Give the extent of all Plasmodium falciparum-infected red blood cells.
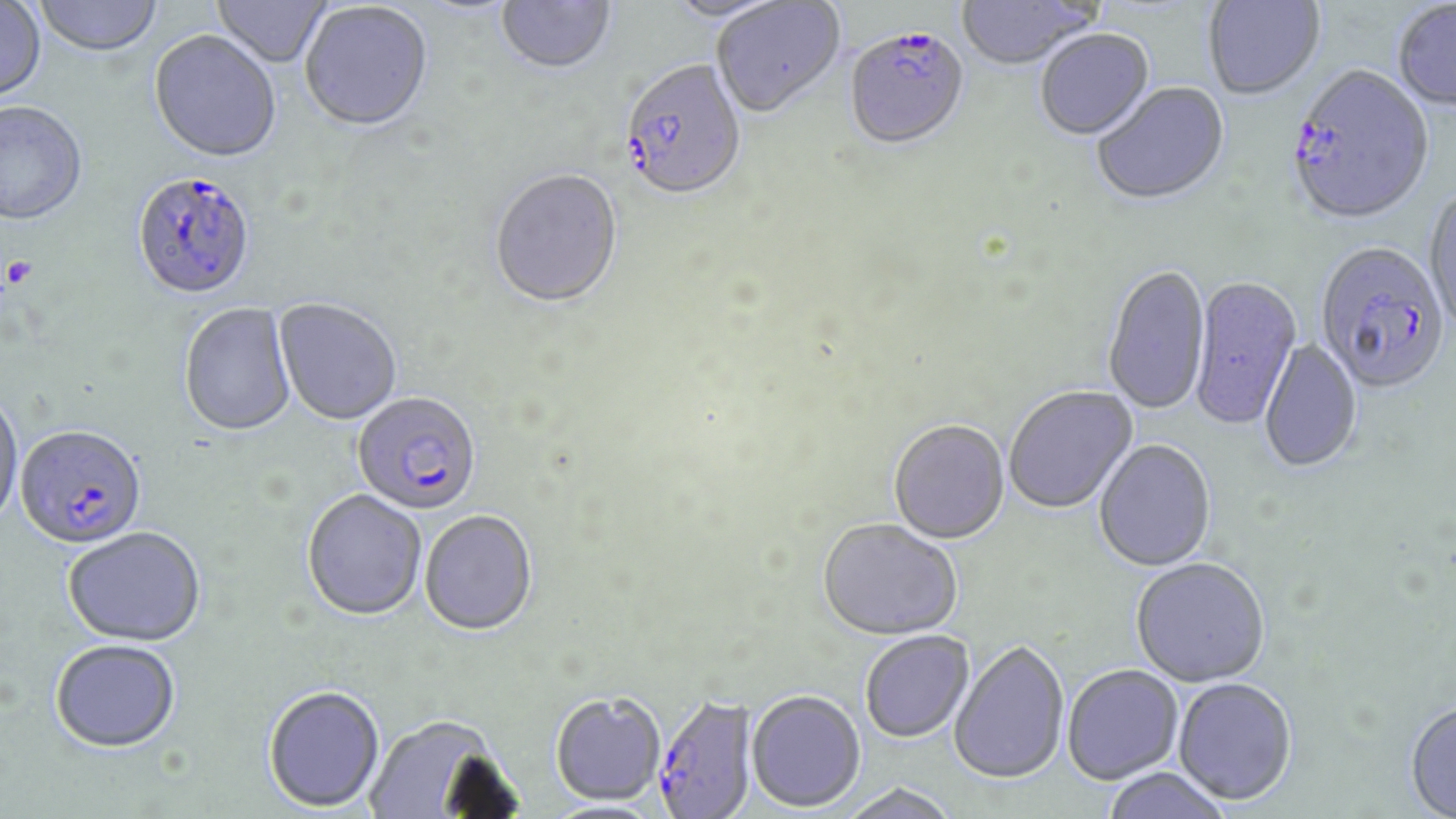

Approximate bounding boxes as named x1/y1/x2/y2 corners in pixels.
Plasmodium falciparum-infected red blood cells: (x1=844, y1=30, x2=969, y2=153), (x1=619, y1=62, x2=748, y2=205), (x1=1285, y1=68, x2=1434, y2=229), (x1=131, y1=174, x2=257, y2=303), (x1=1315, y1=244, x2=1450, y2=398), (x1=352, y1=394, x2=482, y2=517), (x1=15, y1=427, x2=147, y2=552), (x1=652, y1=694, x2=758, y2=818).

Summary:
  - Platelet locations: (x1=1, y1=257, x2=36, y2=292)
  - Uninfected red blood cell locations: (x1=210, y1=0, x2=333, y2=70), (x1=496, y1=0, x2=616, y2=78), (x1=662, y1=0, x2=791, y2=26), (x1=956, y1=0, x2=1101, y2=72), (x1=1204, y1=0, x2=1325, y2=102), (x1=34, y1=1, x2=164, y2=59), (x1=410, y1=1, x2=525, y2=20), (x1=711, y1=1, x2=845, y2=121), (x1=0, y1=2, x2=46, y2=104), (x1=1392, y1=2, x2=1456, y2=114), (x1=300, y1=3, x2=433, y2=135), (x1=1035, y1=30, x2=1155, y2=142), (x1=149, y1=33, x2=281, y2=166), (x1=1092, y1=83, x2=1230, y2=208), (x1=0, y1=104, x2=88, y2=229), (x1=489, y1=171, x2=624, y2=311), (x1=1424, y1=188, x2=1456, y2=335), (x1=1102, y1=267, x2=1211, y2=418), (x1=1188, y1=277, x2=1302, y2=433), (x1=274, y1=299, x2=402, y2=427), (x1=179, y1=304, x2=297, y2=439), (x1=1260, y1=338, x2=1362, y2=474), (x1=1004, y1=386, x2=1138, y2=515), (x1=0, y1=391, x2=25, y2=533), (x1=888, y1=421, x2=1010, y2=545), (x1=1094, y1=440, x2=1216, y2=573), (x1=302, y1=491, x2=426, y2=623), (x1=420, y1=512, x2=538, y2=638), (x1=817, y1=519, x2=963, y2=641), (x1=63, y1=529, x2=206, y2=649), (x1=1130, y1=558, x2=1270, y2=688), (x1=859, y1=630, x2=974, y2=742), (x1=949, y1=640, x2=1070, y2=784), (x1=50, y1=641, x2=181, y2=755), (x1=1062, y1=664, x2=1184, y2=784), (x1=1173, y1=677, x2=1297, y2=805), (x1=263, y1=687, x2=385, y2=814), (x1=747, y1=689, x2=866, y2=813), (x1=551, y1=691, x2=665, y2=806), (x1=1404, y1=700, x2=1456, y2=818), (x1=365, y1=715, x2=506, y2=818), (x1=1101, y1=767, x2=1232, y2=819), (x1=838, y1=783, x2=961, y2=819)
  - Slide-level diagnosis: Plasmodium falciparum
  - Field of view: one of a larger specimen
  - Modality: light microscopy
  - Image size: 1456×819 pixels
  - Magnification: 1000x
  - Stain: May-Grünwald-Giemsa
  - Preparation: thin blood smear